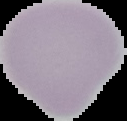
Summary:
  - Malaria status: uninfected
  - Image type: segmented cell region with the area outside set to black
  - Image size: 127×121 pixels
  - Preparation: thin blood film